Classify this cell by malaria status.
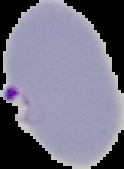
Parasitized.

Segmented cell region on a black background. From a thin blood smear. Image is 124×169 pixels.